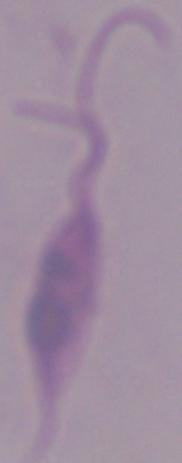

Summary:
  - Magnification: 1000x
  - Identification: Leishmania
  - Modality: micrograph